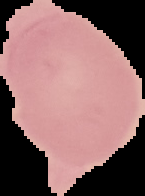

Summary:
  - Preparation: thin blood smear
  - Image size: 145×196 pixels
  - Malaria status: uninfected
  - Image type: cell region segmented out of the field of view; surrounding area masked to black